Classify the preparation.
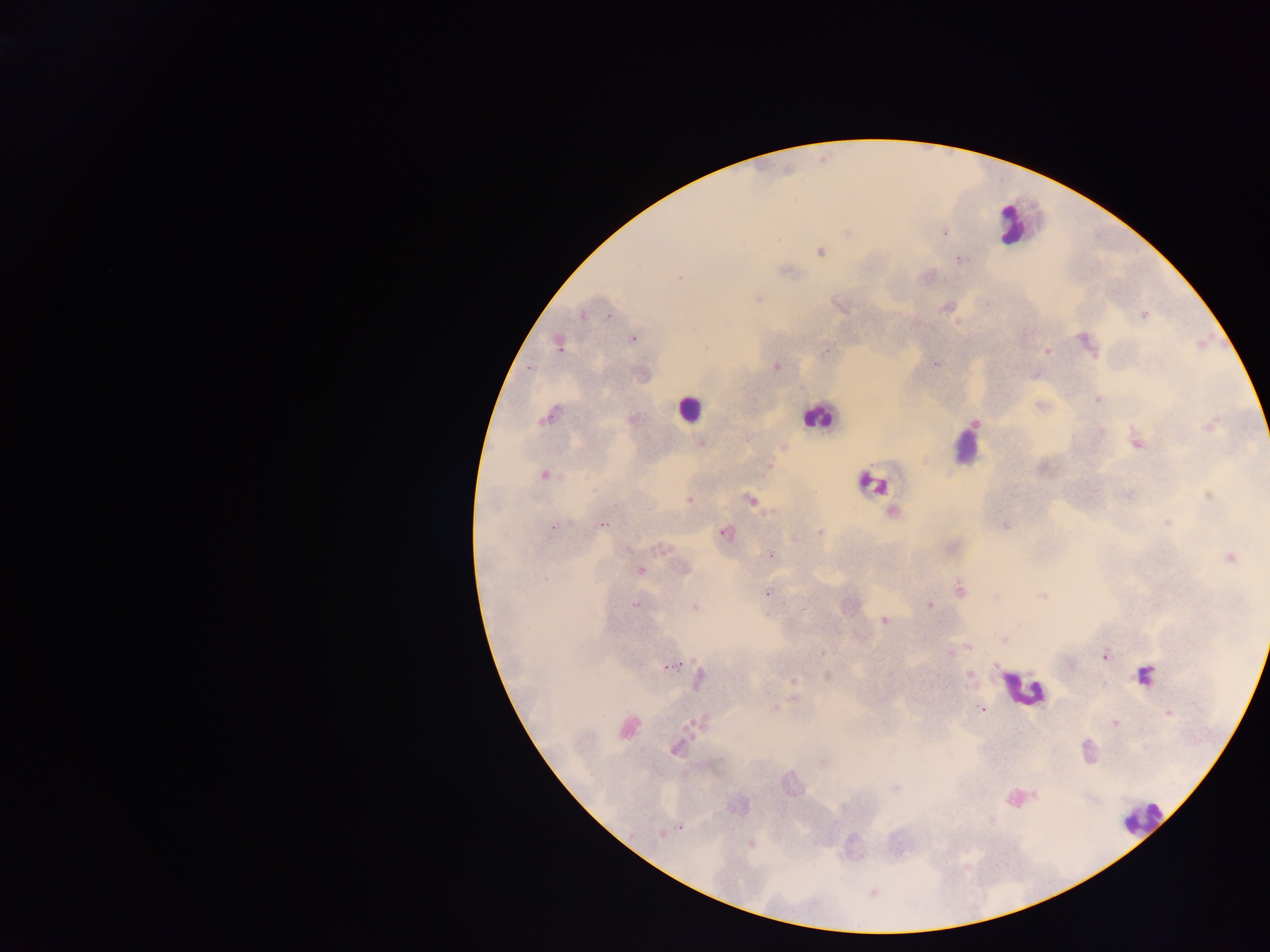
Thick blood film.

image size = 1270×952 pixels
leukocyte locations = approximate centers as {x, y} in pixels: {1013, 224}, {689, 408}, {817, 416}, {965, 443}, {872, 483}, {1145, 676}, {1024, 690}, {1021, 797}, {1140, 817}
Plasmodium parasite locations = approximate centers as {x, y} in pixels: {847, 232}, {944, 232}, {819, 251}, {958, 259}, {786, 270}, {927, 277}, {757, 297}, {840, 306}, {947, 306}, {583, 313}, {1143, 314}, {607, 315}, {632, 338}, {1085, 341}, {558, 343}, {1047, 351}, {825, 352}, {934, 362}, {775, 366}, {529, 368}, {1035, 374}, {1098, 399}, {1041, 407}, {548, 414}, {632, 418}, {1210, 425}, {1098, 432}, {1136, 441}, {701, 442}, {782, 447}, {768, 466}, {1041, 468}, {544, 475}, {1128, 495}, {1209, 495}, {689, 500}, {749, 500}, {892, 513}, {1168, 521}, {601, 524}, {1004, 525}, {552, 527}, {725, 532}, {820, 533}, {662, 549}, {771, 554}, {1229, 557}, {685, 569}, {640, 570}, {959, 590}, {766, 592}, {1042, 596}, {995, 597}, {635, 605}, {930, 605}, {694, 607}, {884, 620}, {1004, 639}, {968, 646}, {948, 654}, {1105, 656}, {673, 665}, {994, 665}, {969, 674}, {829, 676}, {698, 679}, {793, 680}, {793, 697}, {981, 708}, {773, 709}, {1168, 712}, {697, 721}, {1115, 723}, {627, 727}, {676, 748}, {823, 761}, {895, 788}, {680, 828}, {661, 834}, {749, 843}, {872, 892}
country = Ghana
capture = mobile-phone photograph through a microscope
field of view = single